Report the malaria status of this cell.
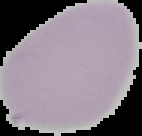

Uninfected.

From a thin blood film. The area outside the segmented cell region is set to black. Image is 142×136 pixels.